Assess the morphology of the red blood cells.
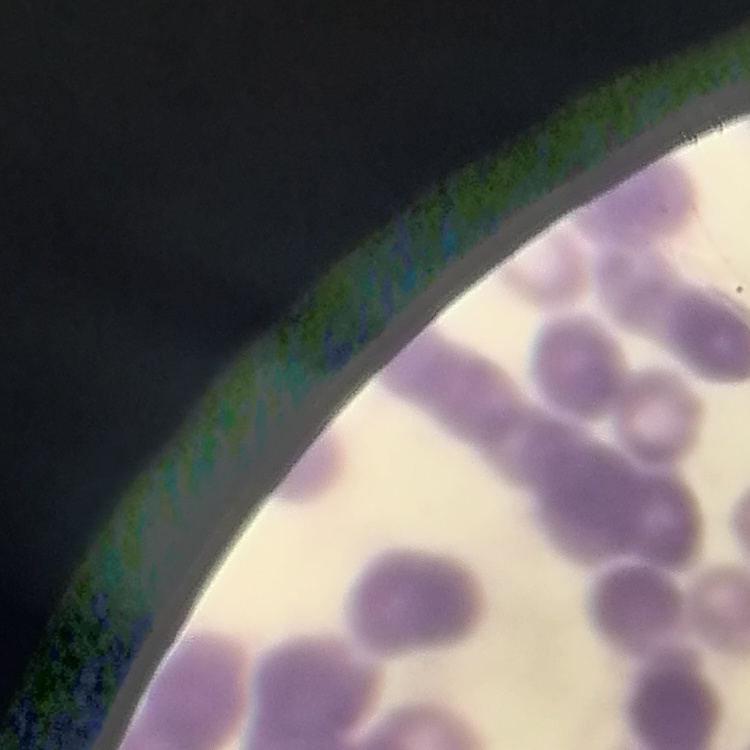

They show rouleaux formation.

stain = Field's or Giemsa
preparation = thin blood smear
image type = square crop of a larger photomicrograph